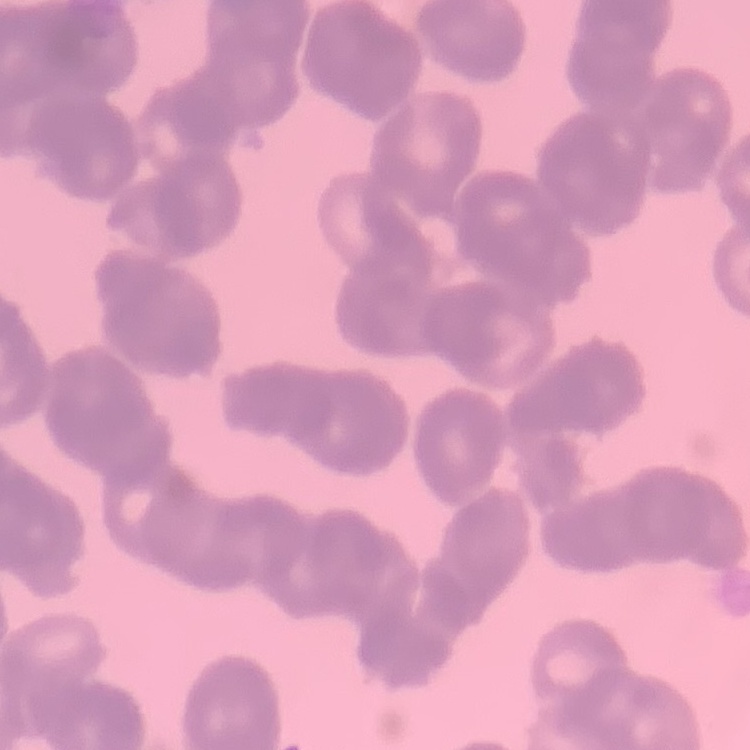

red blood cell morphology = rouleaux formation
stain = Field's or Giemsa
preparation = thin blood smear
image type = square crop of a larger photomicrograph